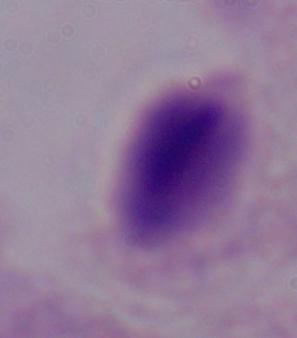

identification = trichomonad
magnification = 1000x
modality = photomicrograph